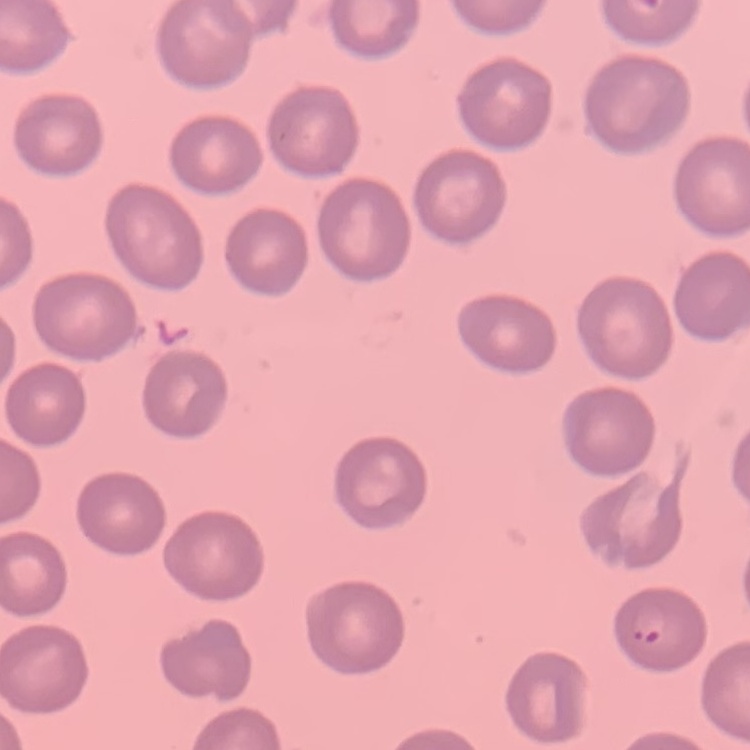
Summary:
  - Erythrocyte morphology: no rouleaux formation
  - Image type: one tile cut from a larger photomicrograph
  - Stain: Field's or Giemsa
  - Preparation: thin blood film